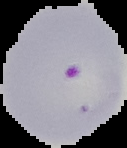

image size = 127×148 pixels
preparation = thin blood film
result = Plasmodium parasites detected
image type = segmented cell region with the area outside set to black